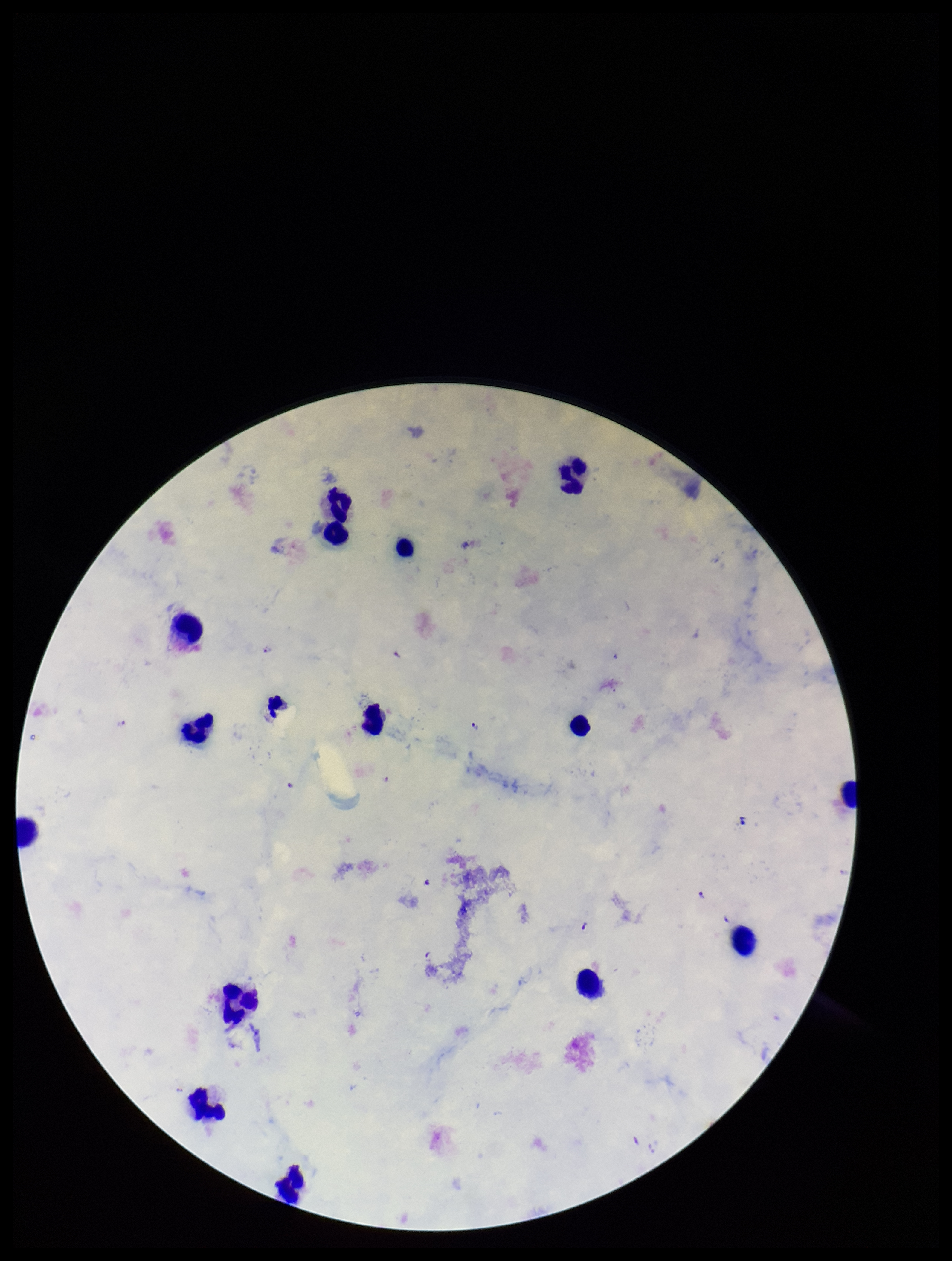

field of view = single
capture = smartphone photograph through the microscope eyepiece
Plasmodium parasites = identified
image size = 952×1261 pixels
leukocyte count = 15
preparation = thick blood smear
stain = Giemsa
patient malaria status = infected
parasite count = 6
species reported for this patient = Plasmodium falciparum